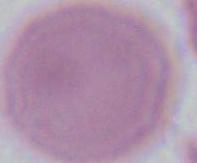

An erythrocyte is seen. Micrograph. 1000x magnification.